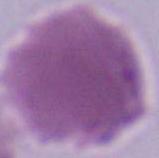 An erythrocyte is seen. Captured at 1000x magnification. Photomicrograph.